Locate every Plasmodium falciparum-infected red blood cell.
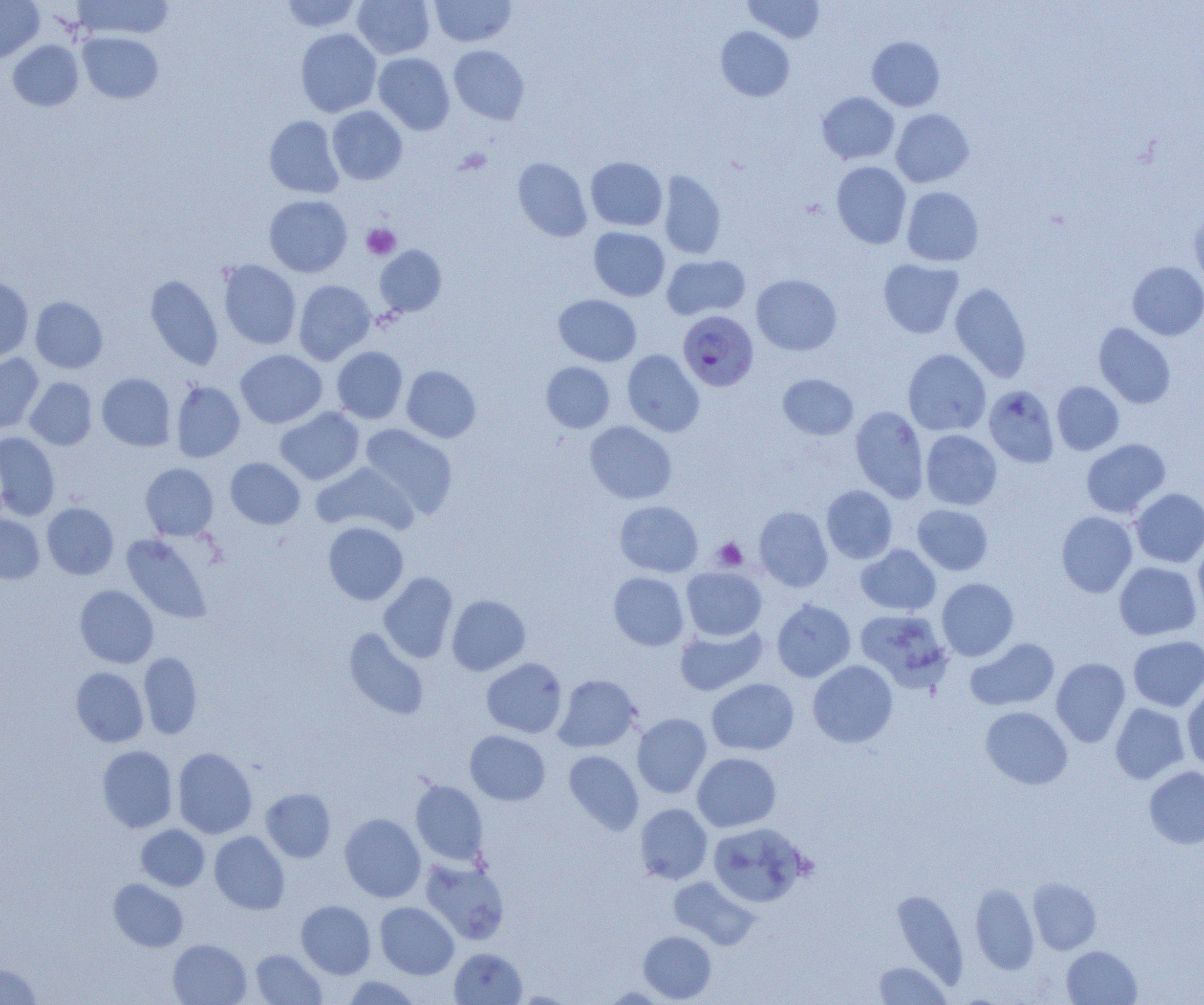

Approximate bounding boxes as [x1, y1, x2, y2] in pixels.
Plasmodium falciparum-infected red blood cells: [677, 311, 758, 391].

{
  "slide_level_diagnosis": "Plasmodium falciparum",
  "modality": "optical microscopy",
  "field_of_view": "single",
  "platelet_locations": "approximate bounding boxes as [x1, y1, x2, y2] in pixels: [361, 224, 401, 260], [712, 538, 748, 571]",
  "uninfected_red_blood_cell_locations": "approximate bounding boxes as [x1, y1, x2, y2] in pixels: [73, 0, 174, 39], [281, 0, 362, 33], [352, 0, 435, 59], [430, 0, 516, 47], [744, 0, 826, 43], [0, 1, 44, 63], [715, 26, 794, 101], [296, 28, 381, 117], [78, 32, 164, 103], [867, 36, 945, 111], [8, 40, 83, 111], [449, 45, 529, 124], [373, 53, 455, 134], [817, 92, 900, 164], [327, 106, 407, 185], [891, 109, 974, 187], [265, 115, 344, 198], [513, 157, 591, 242], [585, 157, 667, 231], [831, 162, 911, 248], [658, 170, 726, 259], [902, 186, 984, 266], [264, 194, 352, 277], [1188, 208, 1204, 292], [589, 227, 669, 301], [375, 245, 447, 316], [662, 255, 750, 320], [878, 258, 964, 338], [218, 260, 301, 349], [1127, 261, 1204, 340], [145, 274, 223, 370], [751, 274, 841, 355], [0, 277, 34, 362], [294, 280, 376, 364], [949, 282, 1032, 383], [553, 294, 642, 366], [30, 296, 108, 373], [1094, 323, 1176, 409], [332, 346, 408, 424], [235, 349, 327, 428], [622, 349, 704, 437], [903, 349, 991, 436], [0, 353, 43, 433], [541, 362, 615, 433], [402, 366, 481, 443], [97, 373, 175, 451], [778, 373, 858, 440], [25, 377, 97, 450], [171, 381, 245, 462], [1052, 381, 1124, 455], [983, 385, 1060, 468], [850, 405, 929, 503], [275, 407, 365, 485], [585, 421, 677, 504], [359, 423, 458, 517], [921, 430, 1002, 510], [0, 432, 60, 520], [1081, 439, 1171, 518], [225, 457, 305, 529], [311, 462, 418, 536], [140, 463, 218, 540], [822, 485, 897, 564], [1130, 488, 1204, 567], [614, 500, 703, 577], [42, 502, 119, 579], [912, 504, 993, 575], [754, 506, 833, 591], [1056, 511, 1137, 597], [0, 513, 45, 584], [323, 521, 409, 605], [122, 534, 213, 624], [1193, 536, 1204, 617], [856, 544, 941, 615], [1114, 561, 1201, 640], [681, 567, 766, 640], [378, 572, 458, 663], [609, 572, 689, 651], [936, 577, 1018, 661], [75, 585, 158, 668], [447, 594, 530, 675], [771, 599, 856, 682], [855, 609, 953, 692], [674, 624, 767, 696], [343, 627, 429, 720], [1128, 635, 1204, 712], [965, 638, 1060, 711], [139, 652, 202, 739], [481, 657, 568, 738], [1051, 657, 1130, 747], [808, 660, 898, 748], [71, 667, 149, 747], [553, 674, 641, 752], [707, 678, 799, 755], [1182, 680, 1204, 772], [1110, 702, 1190, 784], [980, 706, 1072, 789], [632, 713, 711, 798], [465, 730, 550, 805], [97, 745, 177, 832], [173, 747, 257, 838], [563, 750, 643, 835], [692, 753, 781, 832], [1144, 766, 1204, 849], [411, 780, 488, 865], [261, 788, 336, 862], [635, 803, 712, 884], [339, 814, 425, 902], [708, 822, 808, 907], [136, 824, 210, 891], [209, 831, 290, 914], [420, 858, 510, 945], [669, 876, 761, 950], [1028, 877, 1101, 954], [109, 879, 188, 952], [970, 883, 1039, 974], [891, 889, 969, 987], [296, 900, 376, 978], [375, 902, 459, 979], [638, 930, 717, 1003], [168, 939, 251, 1005], [1062, 945, 1142, 1005], [251, 948, 326, 1004], [449, 948, 527, 1004], [0, 961, 43, 1004], [873, 961, 951, 1004], [341, 976, 423, 1004], [600, 986, 672, 1003]",
  "image_size": "1204×1005 pixels",
  "magnification": "1000x",
  "preparation": "thin blood film"
}